Name the cell type shown.
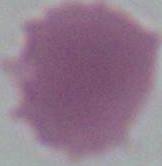

This is an erythrocyte.

magnification = 1000x
modality = photomicrograph